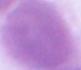

identification = red blood cell
modality = micrograph
magnification = 1000x